Mark where platelets are.
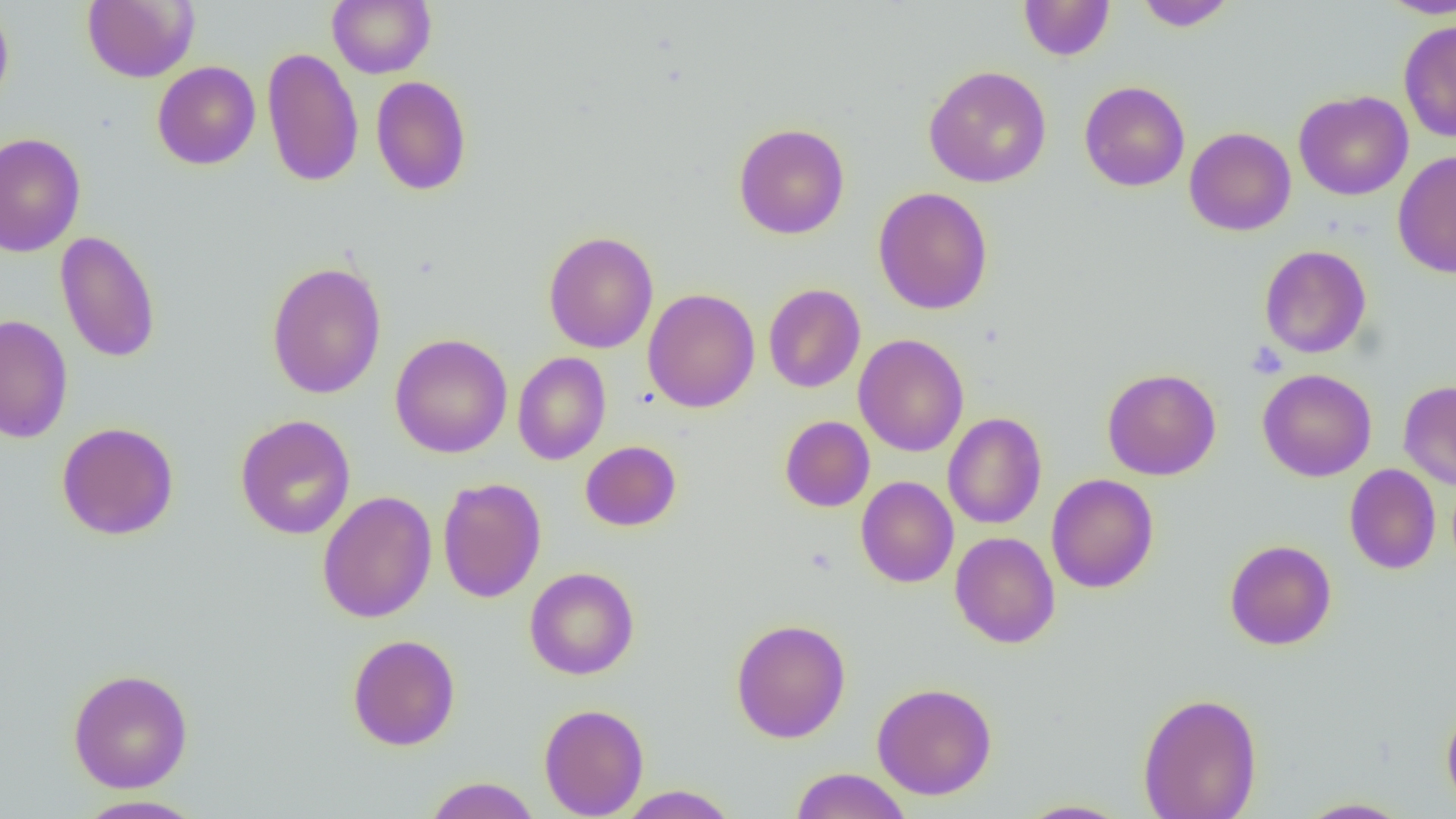
Approximate bounding boxes as named x1/y1/x2/y2 corners in pixels.
Platelets: (x1=1247, y1=342, x2=1288, y2=378).

Summary:
  - Uninfected red blood cell locations: (x1=328, y1=0, x2=436, y2=78), (x1=1135, y1=0, x2=1236, y2=31), (x1=1378, y1=0, x2=1456, y2=17), (x1=83, y1=1, x2=198, y2=83), (x1=1018, y1=1, x2=1115, y2=61), (x1=0, y1=2, x2=14, y2=113), (x1=1398, y1=19, x2=1456, y2=142), (x1=261, y1=46, x2=364, y2=188), (x1=152, y1=61, x2=261, y2=170), (x1=923, y1=66, x2=1052, y2=188), (x1=371, y1=75, x2=472, y2=196), (x1=1079, y1=81, x2=1190, y2=192), (x1=1293, y1=90, x2=1413, y2=200), (x1=733, y1=122, x2=849, y2=240), (x1=1184, y1=127, x2=1296, y2=236), (x1=0, y1=133, x2=86, y2=258), (x1=1392, y1=149, x2=1456, y2=278), (x1=873, y1=186, x2=993, y2=315), (x1=55, y1=230, x2=161, y2=363), (x1=542, y1=230, x2=659, y2=353), (x1=1259, y1=244, x2=1372, y2=359), (x1=266, y1=261, x2=387, y2=399), (x1=763, y1=283, x2=865, y2=393), (x1=642, y1=288, x2=760, y2=413), (x1=0, y1=314, x2=73, y2=444), (x1=389, y1=333, x2=513, y2=458), (x1=853, y1=334, x2=969, y2=457), (x1=513, y1=352, x2=611, y2=465), (x1=1102, y1=368, x2=1222, y2=480), (x1=1258, y1=369, x2=1377, y2=482), (x1=1398, y1=381, x2=1456, y2=490), (x1=943, y1=412, x2=1047, y2=529), (x1=235, y1=414, x2=356, y2=540), (x1=780, y1=416, x2=875, y2=512), (x1=56, y1=422, x2=179, y2=540), (x1=580, y1=441, x2=681, y2=531), (x1=1344, y1=464, x2=1441, y2=574), (x1=1046, y1=473, x2=1159, y2=593), (x1=856, y1=476, x2=959, y2=588), (x1=437, y1=477, x2=547, y2=603), (x1=317, y1=490, x2=437, y2=624), (x1=950, y1=532, x2=1060, y2=648), (x1=1224, y1=540, x2=1337, y2=650), (x1=524, y1=566, x2=639, y2=680), (x1=730, y1=618, x2=851, y2=743), (x1=347, y1=634, x2=461, y2=751), (x1=67, y1=668, x2=194, y2=794), (x1=872, y1=682, x2=997, y2=800), (x1=1138, y1=691, x2=1263, y2=819), (x1=539, y1=702, x2=649, y2=818), (x1=1441, y1=703, x2=1456, y2=814), (x1=790, y1=768, x2=912, y2=819), (x1=425, y1=777, x2=540, y2=819), (x1=616, y1=785, x2=740, y2=818), (x1=72, y1=794, x2=208, y2=818), (x1=1295, y1=798, x2=1413, y2=818), (x1=1015, y1=799, x2=1133, y2=818)
  - Slide-level diagnosis: no evidence of blood parasites
  - Field of view: one of a larger specimen
  - Preparation: thin blood film
  - Modality: optical microscopy
  - Image size: 1456×819 pixels
  - Magnification: 1000x